State the preparation type.
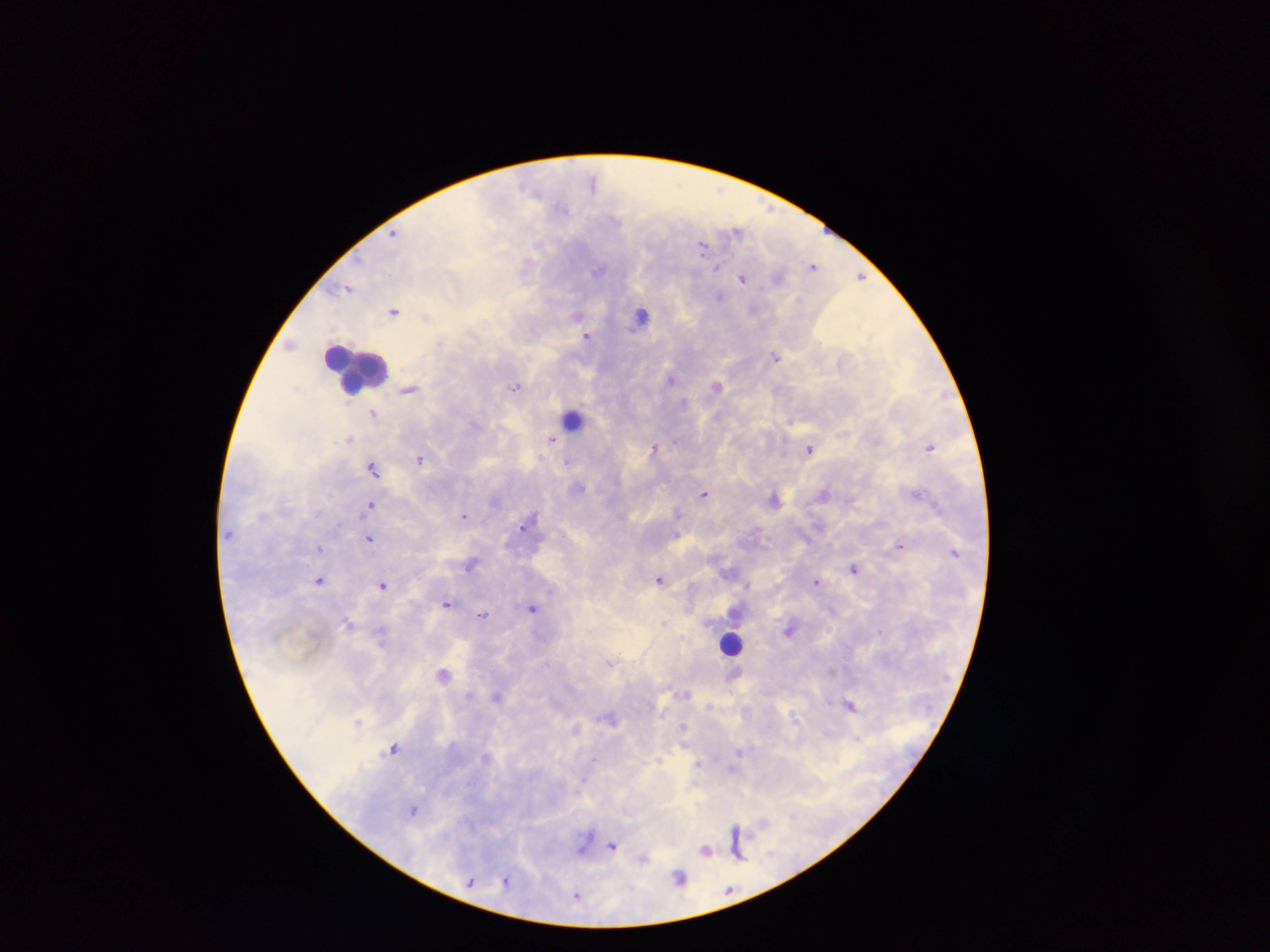

Thick blood smear.

Approximate centers as [x, y] in pixels.
Summary:
  - Malaria parasite locations: [592, 179], [737, 231], [394, 233], [703, 245], [813, 265], [716, 268], [598, 271], [861, 277], [741, 280], [348, 289], [718, 296], [394, 311], [587, 336], [776, 355], [515, 386], [371, 413], [348, 438], [551, 439], [927, 448], [655, 449], [810, 450], [420, 459], [569, 464], [371, 468], [580, 487], [704, 495], [916, 495], [370, 504], [678, 514], [465, 516], [523, 526], [678, 533], [369, 539], [900, 544], [320, 548], [471, 566], [729, 569], [854, 569], [659, 579], [817, 580], [319, 582], [747, 584], [383, 585], [448, 604], [533, 608], [483, 613], [663, 622], [789, 631], [616, 661], [607, 662], [612, 664], [443, 671], [831, 671], [687, 694], [469, 695], [496, 697], [850, 705], [683, 727], [575, 729], [855, 736], [394, 748], [739, 750], [592, 758], [660, 759], [699, 765], [733, 769], [584, 783], [414, 812], [735, 828], [613, 847], [707, 850], [739, 855], [678, 878], [470, 881], [505, 882]
  - Leukocyte locations: [641, 321], [350, 371], [574, 421], [730, 646]
  - Field of view: single
  - Capture: mobile-phone photograph through a microscope
  - Image size: 1270×952 pixels
  - Country: Ghana